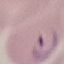
Malaria status: parasitized. Automatically extracted cell patch, resized to 64 × 64 pixels. Photographed with a smartphone camera at the microscope eyepiece. Thin blood smear. Giemsa-stained preparation.